Comment on the morphology of the red blood cells.
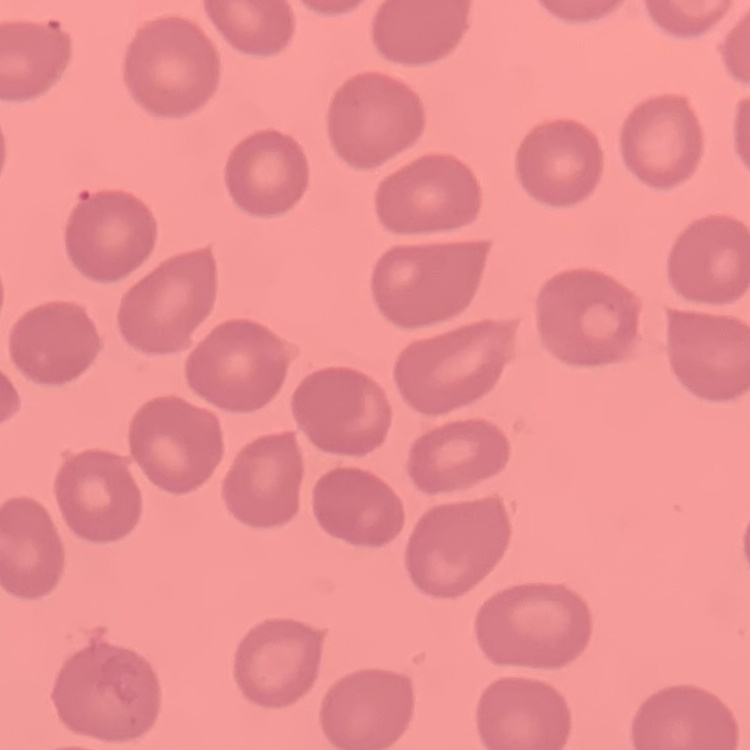

No rouleaux formation.

preparation = thin blood smear
image type = one tile cut from a larger photomicrograph
stain = Field's or Giemsa